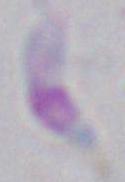
modality = micrograph
magnification = 1000x
identification = Toxoplasma gondii